Classify this cell by malaria status.
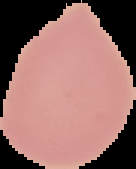

It is uninfected.

Image is 136×169 pixels. From a thin blood smear. Cell region segmented out of the field of view; the surrounding area is masked to black.